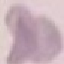
result: no malaria parasites seen
image_type: automatically extracted cell patch, resized to 64 × 64 pixels
capture: smartphone camera at the microscope eyepiece
preparation: thin smear
stain: Giemsa